State the blood parasite species.
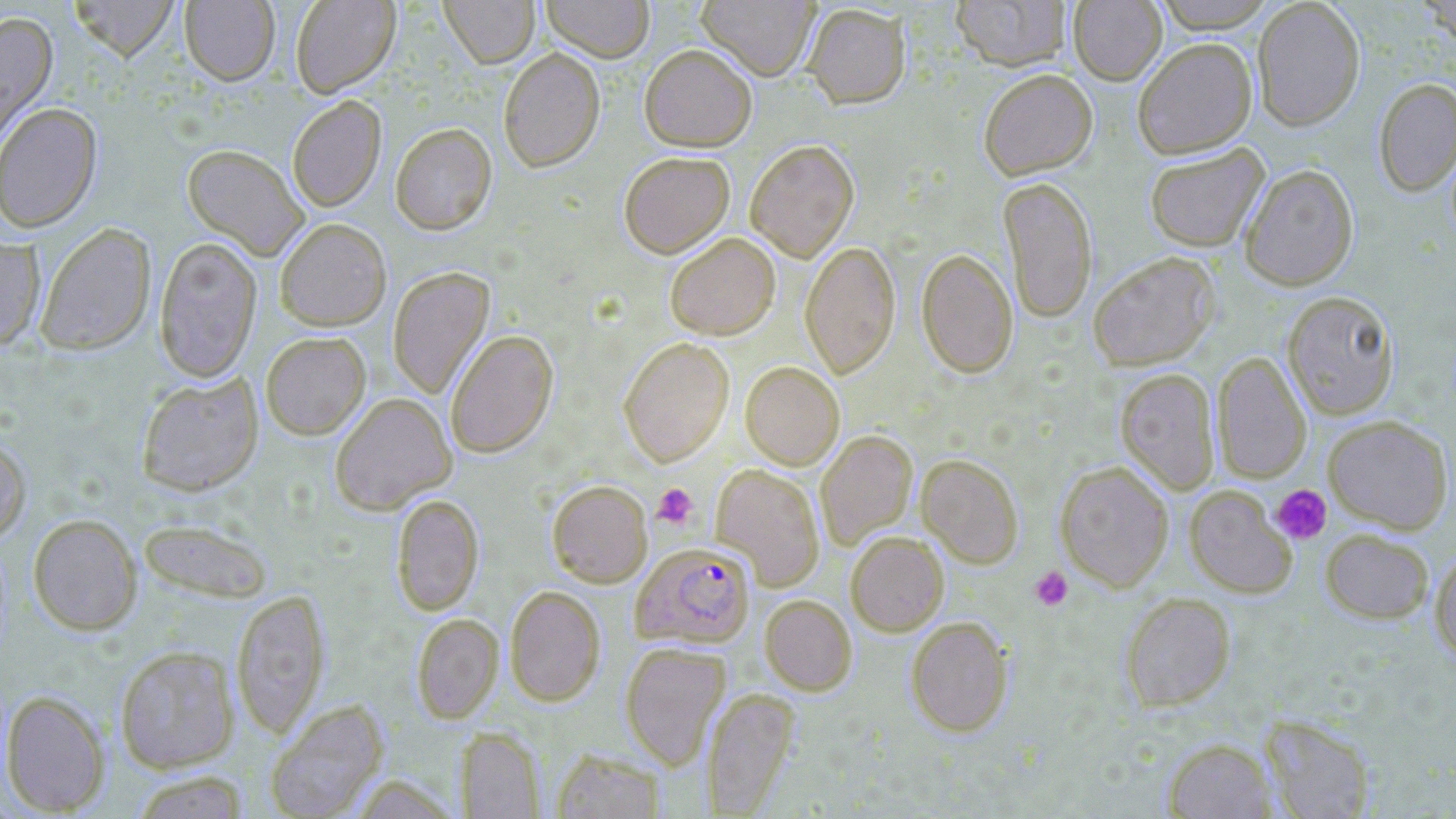

Plasmodium falciparum.

Approximate bounding boxes as [x1, y1, x2, y2] in pixels. Plasmodium falciparum-infected red blood cell locations: [632, 542, 755, 648]. Platelet locations: [651, 482, 699, 530], [1270, 484, 1332, 544], [1029, 565, 1073, 611]. Uninfected red blood cell locations: [68, 0, 180, 60], [290, 0, 400, 98], [440, 0, 539, 68], [541, 0, 654, 62], [696, 0, 819, 81], [951, 0, 1071, 70], [1068, 0, 1166, 85], [1149, 0, 1280, 32], [1252, 0, 1365, 131], [181, 1, 279, 84], [803, 3, 911, 109], [0, 11, 58, 148], [1133, 37, 1257, 159], [639, 43, 757, 151], [498, 47, 605, 172], [979, 68, 1097, 179], [1374, 78, 1456, 198], [287, 95, 386, 212], [1, 102, 102, 233], [390, 122, 496, 234], [745, 139, 859, 262], [182, 143, 310, 260], [1144, 143, 1269, 252], [618, 151, 735, 258], [1240, 164, 1358, 291], [998, 176, 1098, 323], [275, 218, 391, 330], [35, 222, 156, 355], [665, 232, 780, 340], [154, 236, 262, 382], [0, 238, 45, 350], [800, 240, 901, 378], [917, 248, 1018, 378], [1088, 251, 1220, 370], [387, 266, 494, 399], [1282, 290, 1399, 419], [444, 329, 558, 458], [260, 331, 371, 439], [618, 337, 734, 466], [1212, 351, 1312, 483], [740, 360, 844, 469], [1115, 368, 1220, 495], [137, 373, 263, 496], [330, 392, 456, 515], [1323, 415, 1453, 534], [816, 430, 917, 549], [0, 437, 30, 542], [917, 454, 1024, 568], [1055, 460, 1174, 592], [712, 463, 825, 590], [547, 480, 652, 587], [1185, 486, 1296, 598], [390, 495, 484, 616], [28, 514, 142, 635], [138, 517, 274, 602], [1321, 529, 1434, 623], [845, 531, 949, 636], [1430, 548, 1456, 663], [505, 585, 605, 706], [232, 588, 329, 738], [1120, 592, 1235, 711], [760, 594, 857, 695], [412, 614, 503, 723], [905, 616, 1013, 736], [620, 642, 730, 769], [115, 645, 240, 772], [702, 687, 799, 815], [1, 689, 109, 815], [265, 699, 388, 818], [1260, 714, 1377, 818], [456, 728, 545, 818], [1163, 738, 1276, 819], [550, 748, 668, 819], [129, 771, 251, 818]. Optical microscopy. Image is 1456×819 pixels. May-Grünwald-Giemsa stain. Thin blood film. Single field of view. 1000x magnification.